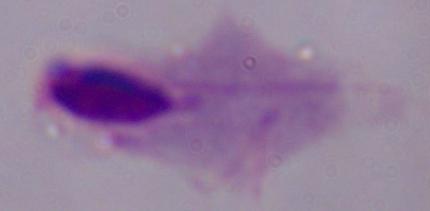 Captured at 1000x magnification. A trichomonad is seen. Photomicrograph.